Name the parasite shown.
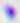
Toxoplasma gondii.

Photomicrograph. 400x magnification.